State the blood parasite species.
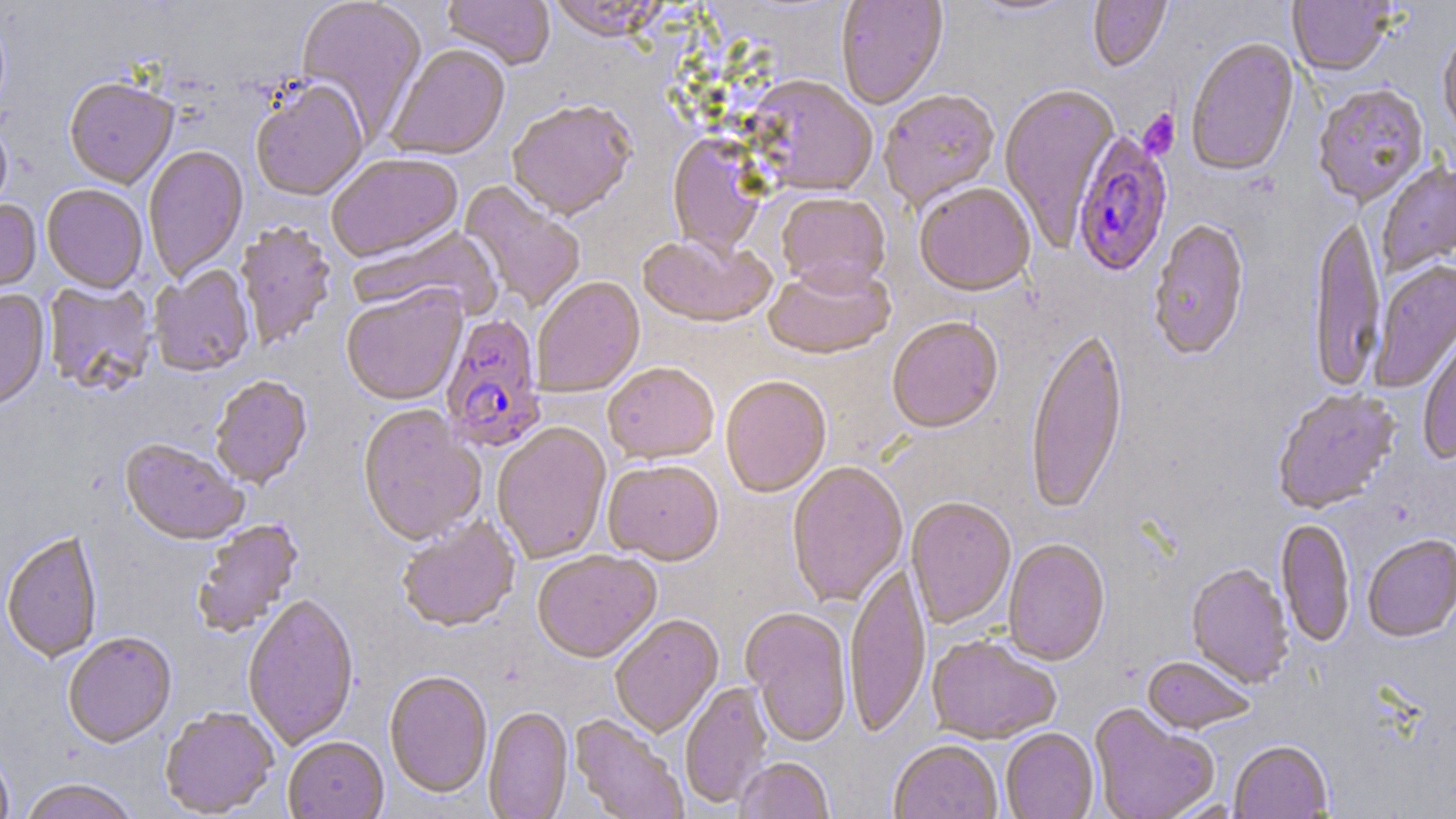
Plasmodium falciparum.

Summary:
  - Coordinate format: approximate bounding boxes as (x1,y1)-(x2,y2) corner pairs in pixels
  - Uninfected red blood cell locations: (294,0)-(428,142), (443,0)-(555,72), (546,0)-(670,45), (835,0)-(948,111), (970,0)-(1083,19), (1088,0)-(1172,74), (1287,0)-(1393,79), (1438,31)-(1456,142), (1186,40)-(1300,180), (386,46)-(510,162), (745,78)-(878,199), (64,80)-(178,191), (250,82)-(369,204), (999,86)-(1120,248), (1313,86)-(1430,209), (879,91)-(1001,213), (507,103)-(636,223), (0,118)-(13,221), (667,134)-(769,259), (143,146)-(249,283), (326,155)-(465,265), (1377,163)-(1456,278), (458,181)-(586,313), (42,186)-(148,294), (915,186)-(1035,300), (775,194)-(891,299), (0,200)-(42,301), (1308,216)-(1385,394), (1148,220)-(1250,362), (235,223)-(337,350), (351,225)-(502,322), (638,235)-(777,332), (1370,261)-(1456,394), (763,265)-(895,363), (149,266)-(255,380), (532,278)-(646,399), (43,282)-(157,398), (341,287)-(468,408), (0,291)-(50,415), (887,319)-(1003,436), (1025,328)-(1129,515), (1418,332)-(1456,463), (602,364)-(719,466), (210,377)-(313,491), (720,379)-(832,500), (1271,390)-(1401,515), (357,407)-(487,549), (492,424)-(612,565), (120,441)-(248,548), (603,462)-(724,568), (787,462)-(909,609), (905,498)-(1016,630), (398,518)-(521,634), (192,519)-(305,638), (1275,520)-(1356,649), (1,533)-(103,664), (1362,536)-(1456,644), (1003,540)-(1110,668), (533,552)-(662,665), (1186,564)-(1294,689), (845,565)-(930,739), (243,596)-(359,750), (741,609)-(853,748), (610,616)-(724,739), (63,634)-(177,749), (926,636)-(1061,745), (1142,657)-(1255,736), (384,671)-(493,799), (680,682)-(773,810), (1088,704)-(1219,819), (483,707)-(573,819), (160,708)-(279,818), (569,715)-(688,818), (1001,729)-(1098,819), (283,737)-(389,819), (1229,741)-(1333,818), (889,742)-(1003,819), (0,749)-(14,819), (734,758)-(835,819), (18,780)-(139,819)
  - Plasmodium falciparum-infected red blood cell locations: (1072,133)-(1173,280), (439,315)-(547,455)
  - Platelet locations: (1139,110)-(1181,161)
  - Field of view: one of a larger specimen
  - Preparation: thin blood smear
  - Magnification: 1000x
  - Modality: optical microscopy
  - Image size: 1456×819 pixels
  - Stain: May-Grünwald-Giemsa